Describe the morphology of the erythrocytes.
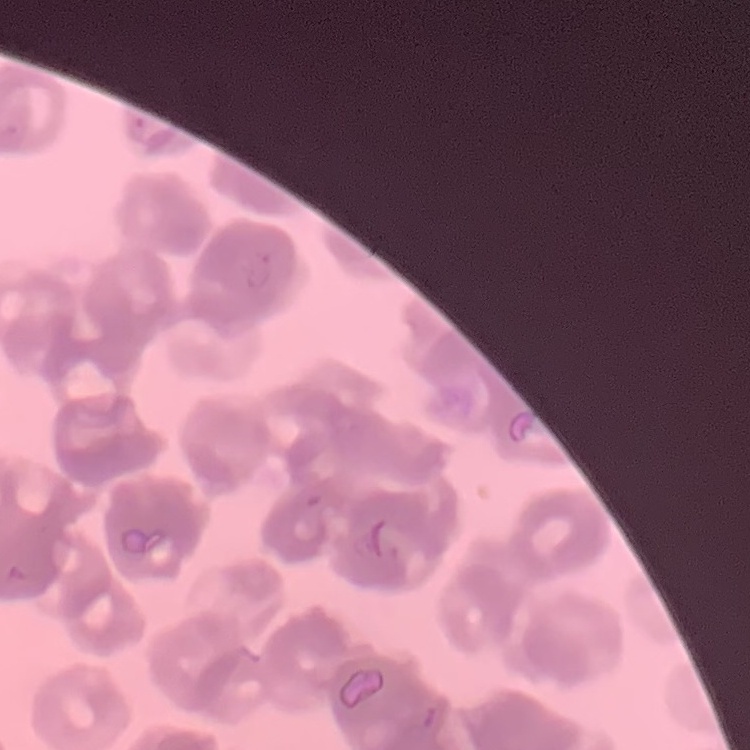

Rouleaux formation.

{
  "preparation": "thin blood smear",
  "image_type": "one tile cut from a larger photomicrograph",
  "stain": "Field's or Giemsa"
}